Assess this cell for malaria.
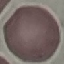
Uninfected.

Summary:
  - Preparation: thin smear
  - Capture: smartphone through the microscope eyepiece
  - Image type: cell patch, automatically extracted from a larger field of view and resized to 64 × 64 pixels
  - Stain: Giemsa